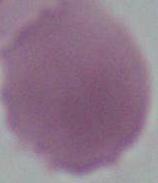

Summary:
  - Identification: red blood cell
  - Magnification: 1000x
  - Modality: micrograph